Identify the cell.
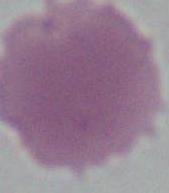
An erythrocyte.

{
  "magnification": "1000x",
  "modality": "micrograph"
}